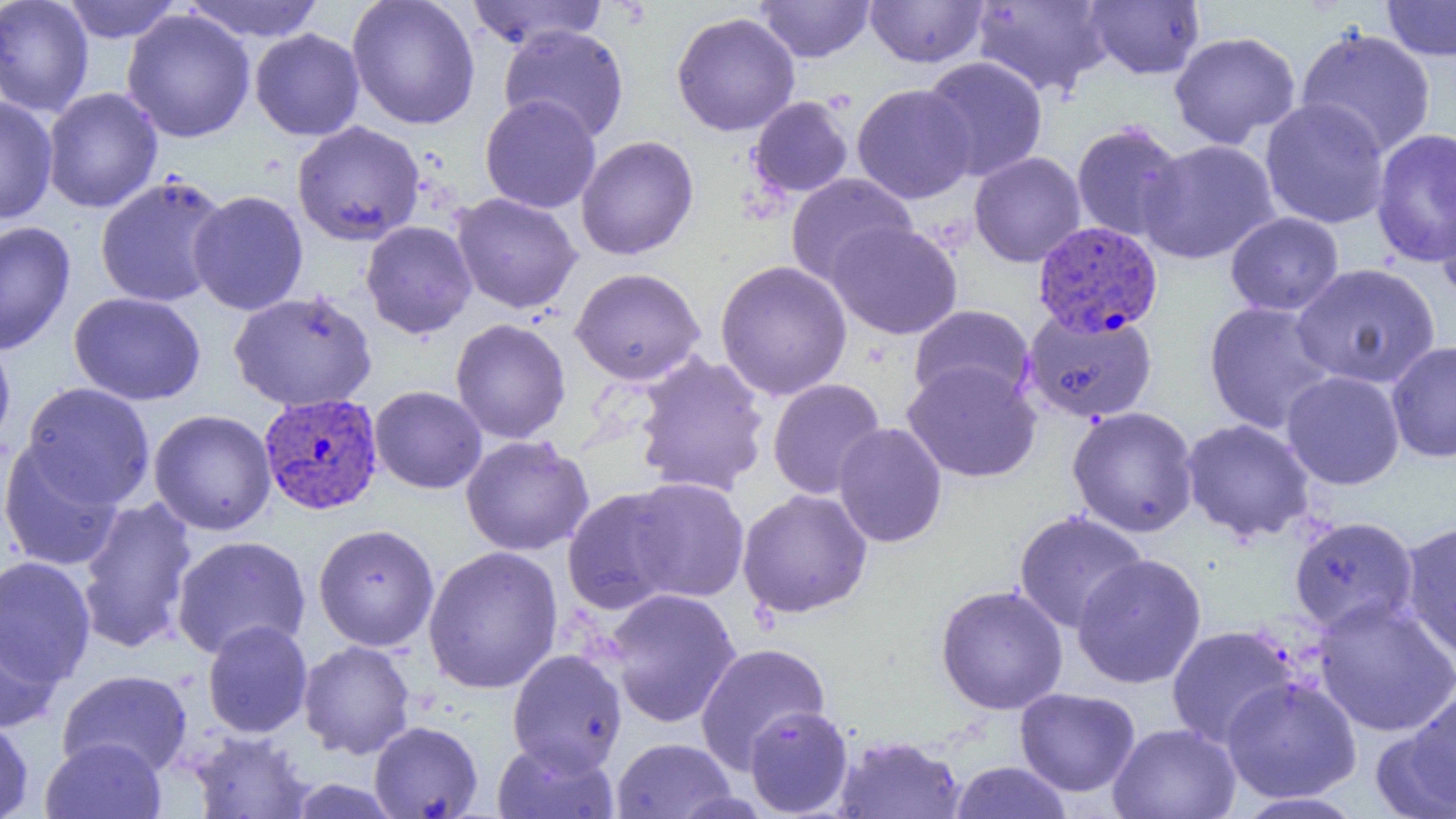
slide-level diagnosis = Plasmodium vivax
preparation = thin blood smear
magnification = 1000x
modality = light microscopy
Plasmodium vivax-infected red blood cell locations = approximate bounding boxes as named x1/y1/x2/y2 corners in pixels: (x1=1032, y1=220, x2=1163, y2=337), (x1=259, y1=393, x2=383, y2=516)
uninfected red blood cell locations = approximate bounding boxes as named x1/y1/x2/y2 corners in pixels: (x1=0, y1=0, x2=94, y2=117), (x1=61, y1=0, x2=182, y2=43), (x1=183, y1=0, x2=326, y2=42), (x1=347, y1=0, x2=481, y2=129), (x1=465, y1=0, x2=609, y2=51), (x1=755, y1=0, x2=875, y2=62), (x1=865, y1=0, x2=989, y2=68), (x1=1381, y1=0, x2=1456, y2=60), (x1=971, y1=1, x2=1112, y2=98), (x1=1085, y1=1, x2=1205, y2=80), (x1=121, y1=9, x2=256, y2=143), (x1=671, y1=11, x2=801, y2=136), (x1=497, y1=24, x2=630, y2=143), (x1=1295, y1=27, x2=1437, y2=159), (x1=250, y1=28, x2=365, y2=141), (x1=1168, y1=30, x2=1301, y2=149), (x1=920, y1=56, x2=1049, y2=182), (x1=851, y1=84, x2=976, y2=204), (x1=42, y1=87, x2=163, y2=213), (x1=480, y1=94, x2=601, y2=213), (x1=0, y1=95, x2=58, y2=225), (x1=748, y1=96, x2=854, y2=198), (x1=1260, y1=98, x2=1390, y2=229), (x1=291, y1=120, x2=425, y2=246), (x1=1070, y1=121, x2=1187, y2=243), (x1=1370, y1=128, x2=1456, y2=267), (x1=576, y1=135, x2=699, y2=261), (x1=1138, y1=139, x2=1280, y2=265), (x1=969, y1=151, x2=1086, y2=267), (x1=785, y1=172, x2=917, y2=288), (x1=95, y1=175, x2=230, y2=309), (x1=1434, y1=188, x2=1455, y2=304), (x1=188, y1=190, x2=308, y2=316), (x1=451, y1=192, x2=583, y2=314), (x1=1225, y1=211, x2=1344, y2=316), (x1=361, y1=220, x2=477, y2=338), (x1=0, y1=221, x2=76, y2=355), (x1=827, y1=221, x2=963, y2=339), (x1=714, y1=259, x2=853, y2=401), (x1=1290, y1=263, x2=1441, y2=389), (x1=569, y1=267, x2=706, y2=386), (x1=228, y1=290, x2=378, y2=412), (x1=68, y1=291, x2=206, y2=406), (x1=1202, y1=301, x2=1338, y2=435), (x1=908, y1=304, x2=1036, y2=407), (x1=1022, y1=307, x2=1158, y2=423), (x1=450, y1=318, x2=571, y2=444), (x1=0, y1=333, x2=16, y2=454), (x1=1386, y1=340, x2=1456, y2=463), (x1=632, y1=351, x2=771, y2=497), (x1=902, y1=360, x2=1042, y2=483), (x1=1281, y1=370, x2=1406, y2=490), (x1=767, y1=378, x2=887, y2=500), (x1=21, y1=382, x2=156, y2=508), (x1=369, y1=385, x2=487, y2=494), (x1=1066, y1=405, x2=1200, y2=538), (x1=148, y1=409, x2=277, y2=536), (x1=1180, y1=418, x2=1317, y2=543), (x1=832, y1=422, x2=948, y2=548), (x1=460, y1=435, x2=594, y2=556), (x1=0, y1=441, x2=124, y2=572), (x1=625, y1=477, x2=751, y2=603), (x1=561, y1=486, x2=687, y2=615), (x1=736, y1=488, x2=873, y2=618), (x1=76, y1=496, x2=199, y2=654), (x1=1013, y1=510, x2=1149, y2=634), (x1=1288, y1=515, x2=1420, y2=636), (x1=1400, y1=520, x2=1456, y2=663), (x1=313, y1=523, x2=440, y2=652), (x1=171, y1=535, x2=311, y2=660), (x1=422, y1=545, x2=564, y2=695), (x1=1071, y1=553, x2=1207, y2=689), (x1=0, y1=556, x2=96, y2=687), (x1=935, y1=584, x2=1069, y2=715), (x1=603, y1=587, x2=742, y2=728), (x1=1313, y1=598, x2=1456, y2=738), (x1=0, y1=616, x2=63, y2=735), (x1=202, y1=620, x2=313, y2=738), (x1=1166, y1=625, x2=1299, y2=749), (x1=298, y1=640, x2=416, y2=759), (x1=694, y1=641, x2=832, y2=773), (x1=506, y1=649, x2=628, y2=775), (x1=57, y1=669, x2=193, y2=778), (x1=1220, y1=676, x2=1362, y2=803), (x1=1015, y1=687, x2=1141, y2=797), (x1=1391, y1=690, x2=1456, y2=814), (x1=743, y1=705, x2=854, y2=817), (x1=0, y1=717, x2=34, y2=819), (x1=369, y1=720, x2=484, y2=818), (x1=1108, y1=722, x2=1242, y2=819), (x1=186, y1=730, x2=316, y2=818), (x1=833, y1=734, x2=966, y2=819), (x1=40, y1=736, x2=167, y2=819), (x1=611, y1=737, x2=737, y2=818), (x1=491, y1=739, x2=620, y2=819), (x1=950, y1=760, x2=1073, y2=818), (x1=285, y1=778, x2=403, y2=818), (x1=1232, y1=792, x2=1368, y2=818)
image size = 1456×819 pixels
field of view = one of a larger specimen